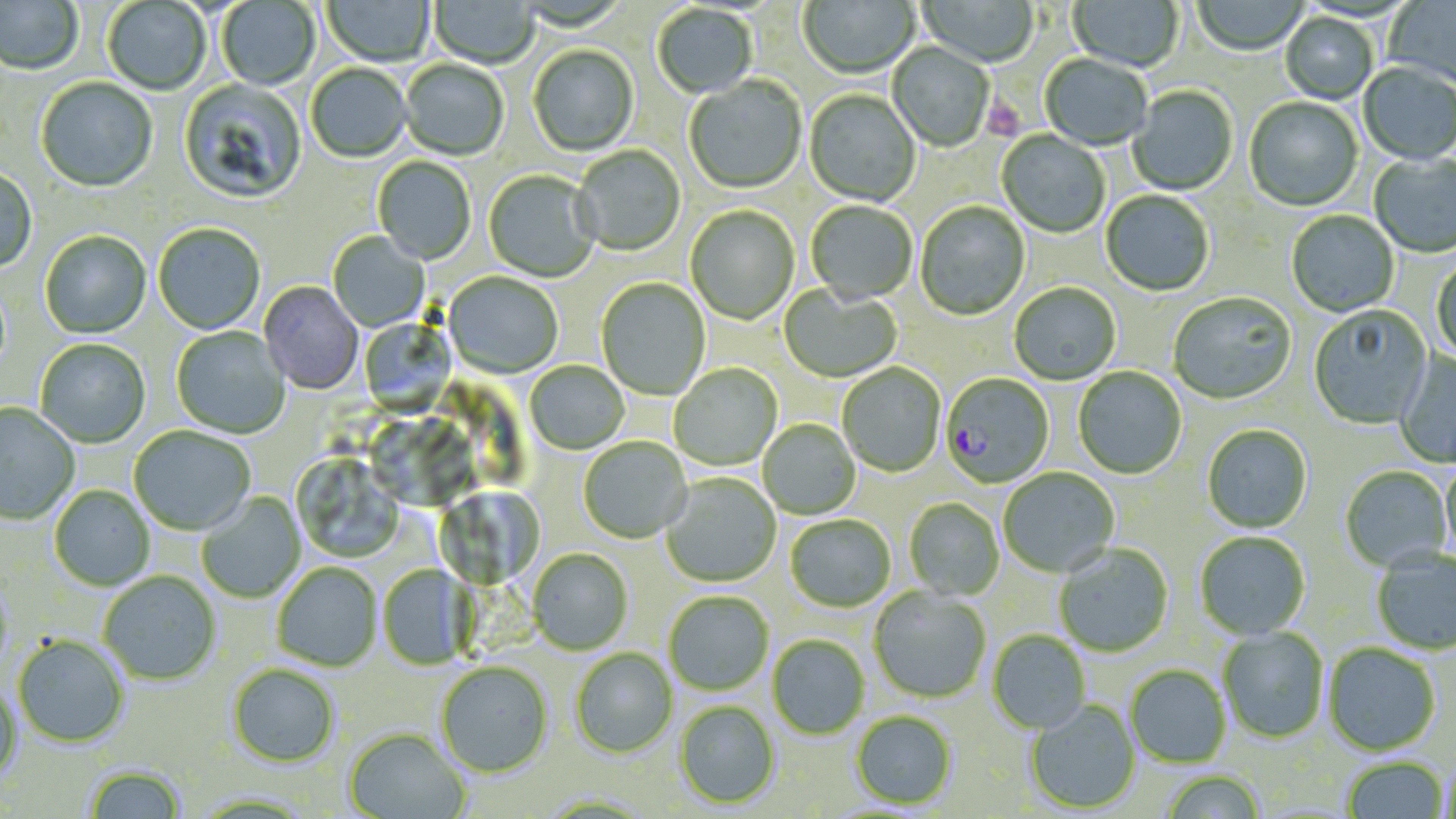

Summary:
  - Coordinate format: approximate bounding boxes as named x1/y1/x2/y2 corners in pixels
  - Uninfected red blood cell locations: (x1=0, y1=0, x2=84, y2=76), (x1=217, y1=0, x2=320, y2=91), (x1=322, y1=0, x2=435, y2=68), (x1=429, y1=0, x2=538, y2=70), (x1=798, y1=0, x2=920, y2=80), (x1=917, y1=0, x2=1038, y2=69), (x1=1067, y1=0, x2=1184, y2=74), (x1=1383, y1=0, x2=1456, y2=90), (x1=102, y1=1, x2=210, y2=96), (x1=1193, y1=1, x2=1308, y2=56), (x1=652, y1=5, x2=757, y2=100), (x1=1280, y1=13, x2=1378, y2=105), (x1=888, y1=43, x2=994, y2=152), (x1=528, y1=46, x2=639, y2=157), (x1=1040, y1=54, x2=1151, y2=152), (x1=400, y1=61, x2=509, y2=162), (x1=1358, y1=63, x2=1456, y2=167), (x1=306, y1=65, x2=411, y2=164), (x1=684, y1=77, x2=807, y2=195), (x1=36, y1=78, x2=158, y2=194), (x1=178, y1=80, x2=307, y2=205), (x1=1128, y1=86, x2=1238, y2=197), (x1=804, y1=90, x2=920, y2=208), (x1=1244, y1=97, x2=1363, y2=212), (x1=997, y1=131, x2=1110, y2=238), (x1=571, y1=146, x2=685, y2=257), (x1=1369, y1=153, x2=1456, y2=260), (x1=373, y1=157, x2=476, y2=265), (x1=0, y1=167, x2=37, y2=273), (x1=483, y1=171, x2=599, y2=283), (x1=1101, y1=191, x2=1214, y2=297), (x1=806, y1=201, x2=917, y2=306), (x1=915, y1=202, x2=1030, y2=321), (x1=685, y1=206, x2=799, y2=325), (x1=1286, y1=210, x2=1399, y2=318), (x1=153, y1=225, x2=266, y2=336), (x1=40, y1=232, x2=152, y2=339), (x1=328, y1=232, x2=430, y2=332), (x1=1431, y1=257, x2=1456, y2=365), (x1=443, y1=273, x2=563, y2=379), (x1=596, y1=278, x2=710, y2=401), (x1=258, y1=282, x2=363, y2=395), (x1=1009, y1=283, x2=1121, y2=386), (x1=779, y1=286, x2=902, y2=383), (x1=1168, y1=293, x2=1296, y2=405), (x1=1308, y1=305, x2=1433, y2=430), (x1=358, y1=317, x2=456, y2=417), (x1=170, y1=326, x2=291, y2=440), (x1=35, y1=340, x2=150, y2=448), (x1=1395, y1=351, x2=1456, y2=468), (x1=525, y1=361, x2=630, y2=455), (x1=837, y1=363, x2=946, y2=478), (x1=669, y1=364, x2=782, y2=471), (x1=1073, y1=367, x2=1187, y2=479), (x1=1, y1=403, x2=80, y2=526), (x1=758, y1=420, x2=860, y2=519), (x1=1201, y1=424, x2=1312, y2=533), (x1=129, y1=426, x2=255, y2=536), (x1=578, y1=437, x2=692, y2=544), (x1=291, y1=454, x2=405, y2=563), (x1=1440, y1=459, x2=1456, y2=565), (x1=1339, y1=466, x2=1452, y2=571), (x1=998, y1=467, x2=1119, y2=578), (x1=661, y1=474, x2=781, y2=588), (x1=49, y1=485, x2=156, y2=591), (x1=196, y1=493, x2=306, y2=603), (x1=904, y1=498, x2=1004, y2=600), (x1=785, y1=515, x2=895, y2=613), (x1=1194, y1=531, x2=1311, y2=640), (x1=1053, y1=543, x2=1173, y2=657), (x1=528, y1=548, x2=633, y2=655), (x1=1371, y1=548, x2=1456, y2=654), (x1=272, y1=563, x2=383, y2=672), (x1=377, y1=564, x2=476, y2=670), (x1=98, y1=571, x2=221, y2=686), (x1=869, y1=587, x2=991, y2=703), (x1=664, y1=591, x2=773, y2=696), (x1=1217, y1=627, x2=1329, y2=743), (x1=987, y1=630, x2=1091, y2=734), (x1=767, y1=635, x2=870, y2=739), (x1=12, y1=636, x2=129, y2=748), (x1=1323, y1=642, x2=1441, y2=755), (x1=570, y1=648, x2=678, y2=758), (x1=436, y1=661, x2=554, y2=777), (x1=227, y1=664, x2=340, y2=768), (x1=1125, y1=664, x2=1230, y2=768), (x1=0, y1=682, x2=22, y2=783), (x1=1025, y1=699, x2=1140, y2=814), (x1=674, y1=701, x2=780, y2=808), (x1=851, y1=710, x2=957, y2=809), (x1=343, y1=728, x2=470, y2=819), (x1=1343, y1=757, x2=1448, y2=817), (x1=83, y1=765, x2=186, y2=819), (x1=1159, y1=770, x2=1267, y2=818)
  - Platelet locations: (x1=981, y1=93, x2=1024, y2=144)
  - Plasmodium falciparum-infected red blood cell locations: (x1=941, y1=374, x2=1054, y2=489)
  - Slide-level diagnosis: Plasmodium falciparum
  - Image size: 1456×819 pixels
  - Field of view: single
  - Magnification: 1000x
  - Stain: May-Grünwald-Giemsa
  - Preparation: thin blood smear
  - Modality: light microscopy